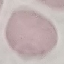
Result: no malaria parasites seen. Giemsa-stained preparation. Thin smear of blood. Photographed with a smartphone camera at the microscope eyepiece. Cell patch, automatically extracted from a larger field of view and resized to 64 × 64 pixels.